Name the parasite shown.
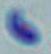
Toxoplasma gondii.

modality = micrograph
magnification = 1000x